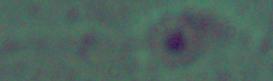

A Leishmania parasite is shown. Captured at 1000x magnification. Photomicrograph.